Assess this cell for malaria.
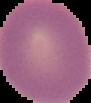

Uninfected.

Segmented cell region on a black background. From a thin blood film. Image is 91×103 pixels.